Assess this cell for malaria.
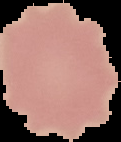
Uninfected.

Summary:
  - Image type: segmented cell region on a black background
  - Preparation: thin blood smear
  - Image size: 121×142 pixels